Give the extent of all Plasmodium ovale-infected red blood cells.
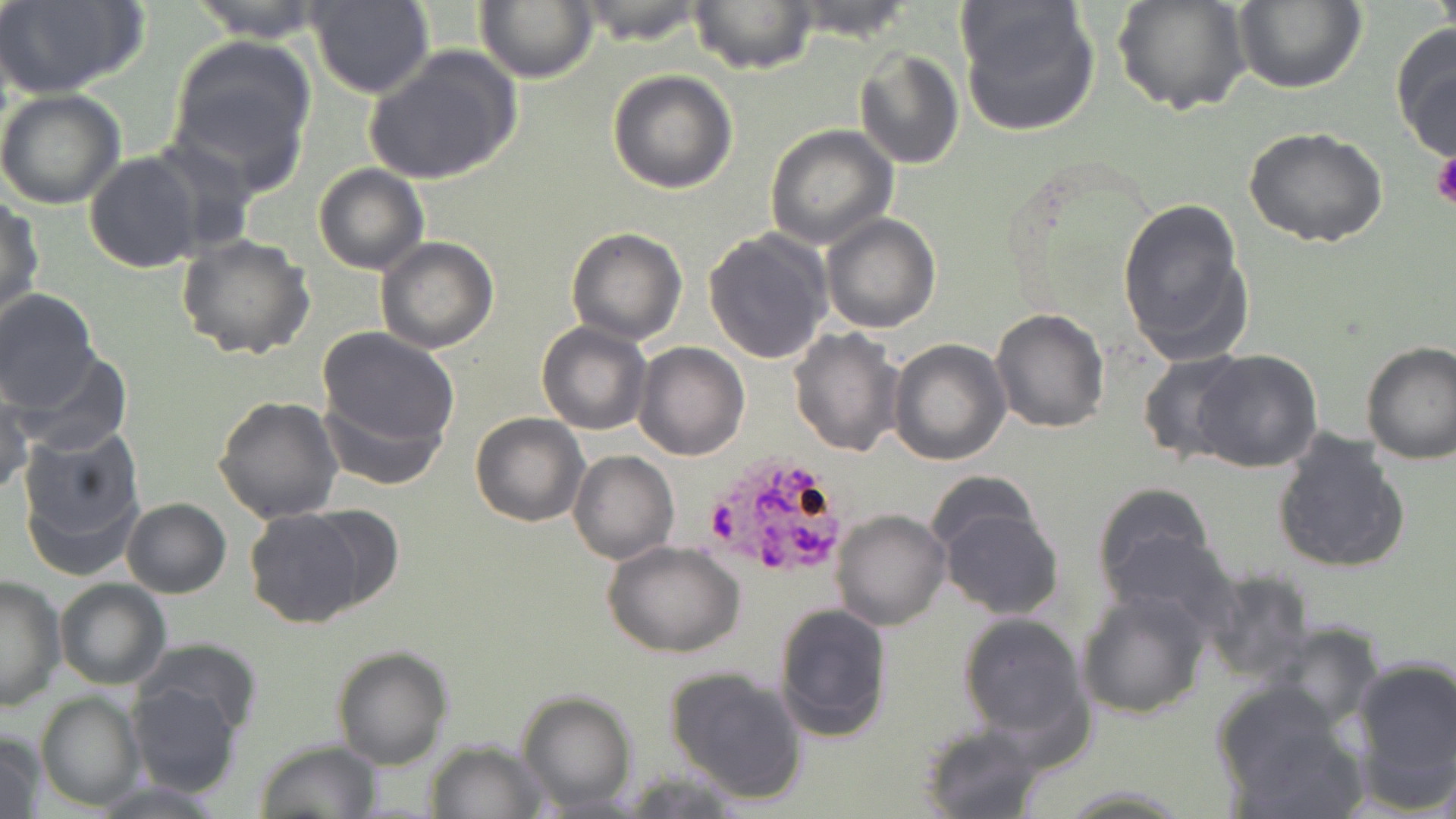

Approximate bounding boxes as (x1, y1, x2, y2) in pixels.
Plasmodium ovale-infected red blood cells: (705, 451, 851, 581).

Platelet locations: (1430, 151, 1456, 211). Uninfected red blood cell locations: (1, 0, 149, 99), (185, 0, 329, 42), (311, 0, 434, 100), (475, 0, 597, 83), (783, 0, 921, 43), (1113, 0, 1253, 119), (1429, 0, 1455, 38), (955, 1, 1100, 137), (1232, 1, 1365, 93), (571, 2, 713, 46), (689, 2, 817, 74), (1390, 21, 1456, 160), (166, 34, 317, 188), (364, 46, 523, 188), (853, 48, 964, 169), (608, 68, 738, 192), (0, 89, 125, 210), (764, 124, 897, 250), (1244, 127, 1389, 248), (84, 150, 206, 274), (314, 164, 428, 275), (1, 196, 43, 321), (1117, 198, 1254, 365), (822, 214, 941, 333), (702, 227, 833, 363), (567, 228, 687, 344), (175, 233, 315, 360), (376, 238, 498, 354), (0, 289, 100, 409), (989, 307, 1110, 432), (536, 321, 652, 436), (788, 327, 905, 459), (317, 329, 459, 451), (888, 338, 1011, 465), (1360, 340, 1456, 463), (632, 343, 749, 461), (1190, 348, 1322, 473), (11, 349, 132, 457), (1136, 350, 1249, 465), (0, 386, 32, 497), (319, 392, 446, 491), (214, 395, 345, 525), (470, 412, 589, 527), (17, 424, 145, 575), (1269, 429, 1411, 574), (569, 449, 678, 564), (925, 473, 1041, 564), (1091, 481, 1220, 609), (121, 498, 231, 598), (297, 504, 406, 615), (936, 505, 1063, 621), (244, 508, 368, 628), (831, 509, 951, 630), (1102, 528, 1240, 634), (604, 542, 745, 657), (1201, 572, 1313, 684), (0, 574, 65, 712), (55, 578, 171, 690), (1076, 589, 1208, 718), (773, 602, 891, 743), (956, 614, 1090, 743), (1258, 622, 1384, 734), (141, 639, 261, 736), (331, 644, 454, 770), (1349, 655, 1456, 808), (663, 665, 810, 805), (129, 682, 240, 797), (1213, 683, 1366, 817), (516, 688, 637, 813), (36, 692, 145, 810), (918, 722, 1051, 818), (1, 730, 46, 818), (254, 740, 382, 818), (424, 741, 547, 819), (88, 779, 229, 816), (1058, 784, 1194, 818). Slide-level diagnosis: Plasmodium ovale. Thin blood smear. Optical microscopy. May-Grünwald-Giemsa stain. Image is 1456×819 pixels. 1000x magnification. One field of a larger specimen.